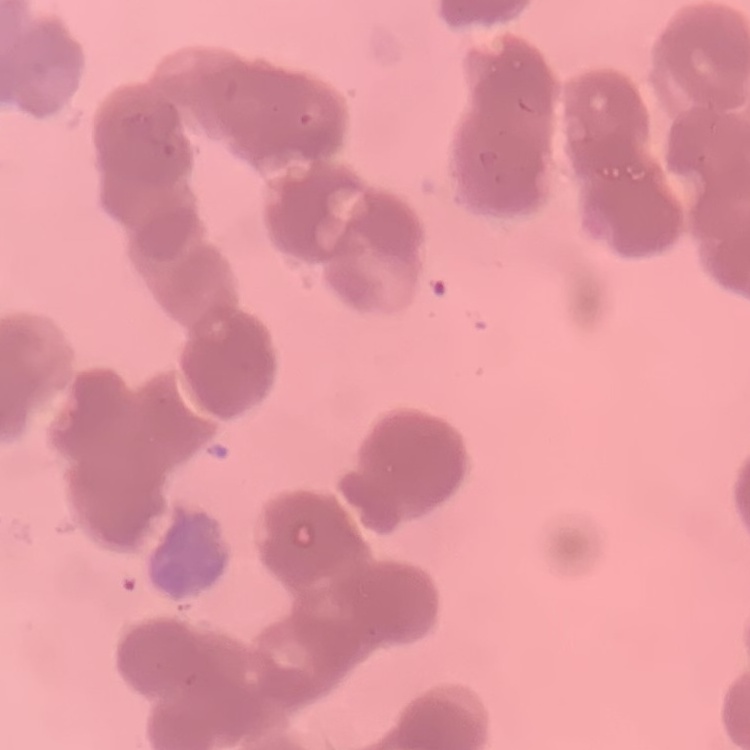
erythrocyte morphology = rouleaux formation
stain = Field's or Giemsa
preparation = thin peripheral smear
image type = square crop of a larger photomicrograph